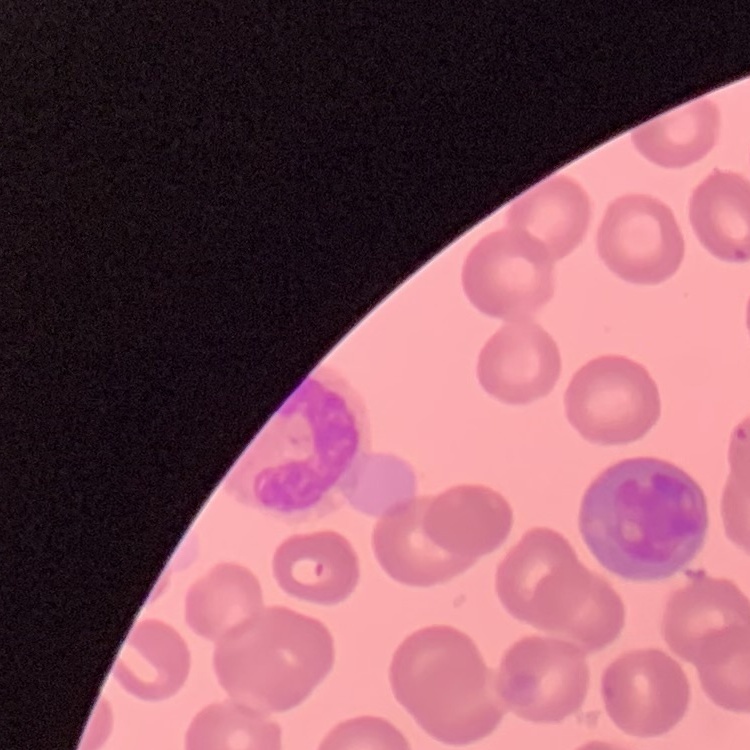
red_blood_cell_morphology: no rouleaux formation
preparation: thin peripheral smear
stain: Field's or Giemsa
image_type: one tile cut from a larger photomicrograph